Name the cell type shown.
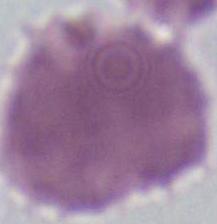

An erythrocyte.

1000x magnification. Photomicrograph.